Name the blood parasite species.
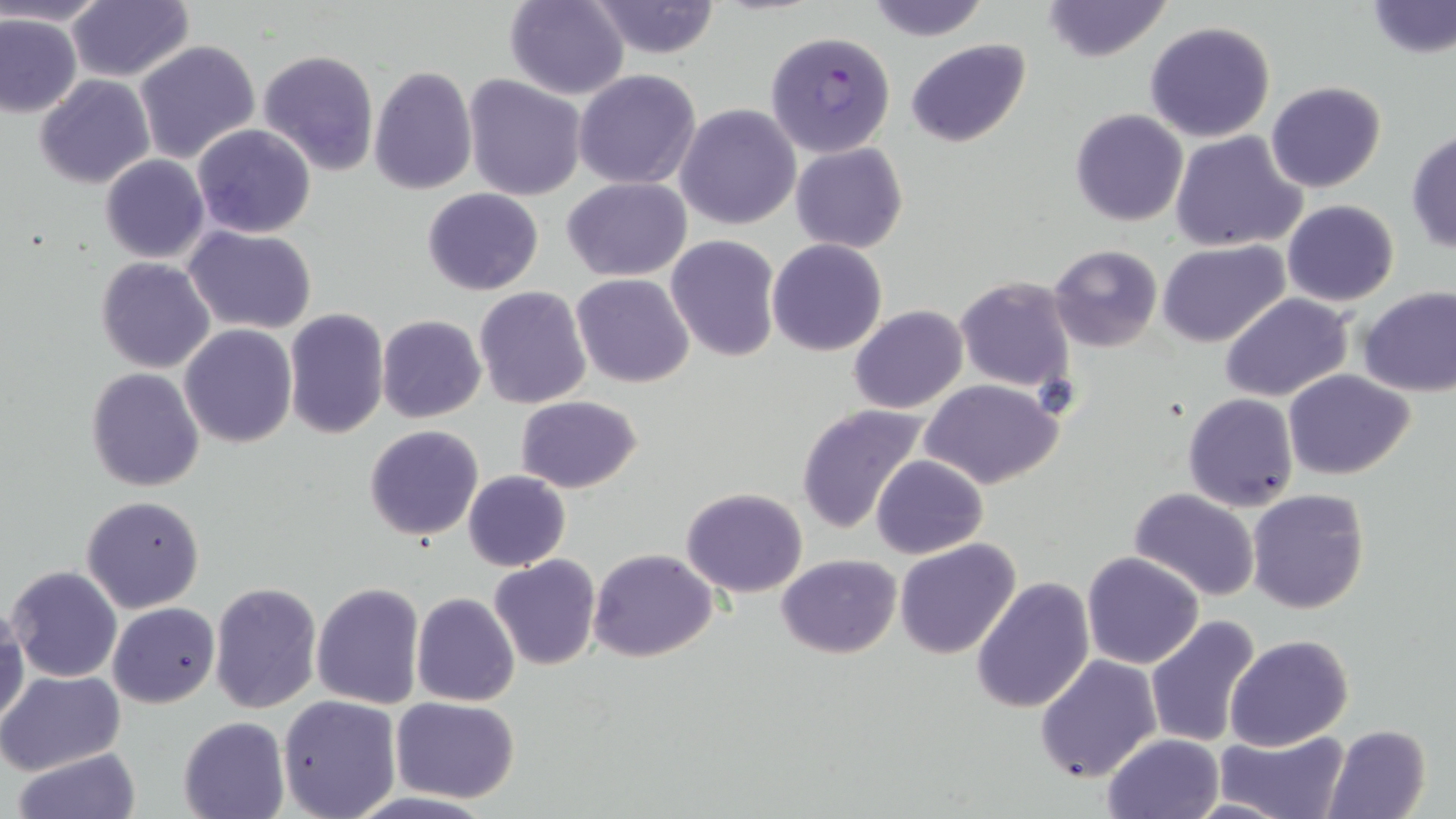

Plasmodium falciparum.

Approximate bounding boxes as named x1/y1/x2/y2 corners in pixels. Plasmodium falciparum-infected red blood cell locations: (x1=764, y1=30, x2=897, y2=160). Uninfected red blood cell locations: (x1=0, y1=0, x2=109, y2=27), (x1=503, y1=0, x2=629, y2=99), (x1=863, y1=0, x2=992, y2=42), (x1=1041, y1=0, x2=1172, y2=62), (x1=1366, y1=0, x2=1455, y2=60), (x1=586, y1=1, x2=723, y2=58), (x1=66, y1=2, x2=193, y2=83), (x1=0, y1=9, x2=82, y2=118), (x1=1144, y1=19, x2=1277, y2=142), (x1=906, y1=38, x2=1030, y2=149), (x1=133, y1=40, x2=260, y2=166), (x1=258, y1=49, x2=380, y2=175), (x1=369, y1=66, x2=477, y2=195), (x1=574, y1=69, x2=702, y2=189), (x1=35, y1=75, x2=154, y2=190), (x1=463, y1=75, x2=587, y2=201), (x1=1266, y1=80, x2=1387, y2=194), (x1=674, y1=103, x2=801, y2=230), (x1=1069, y1=108, x2=1188, y2=227), (x1=191, y1=124, x2=317, y2=239), (x1=1169, y1=129, x2=1309, y2=253), (x1=1406, y1=131, x2=1456, y2=255), (x1=790, y1=142, x2=908, y2=253), (x1=99, y1=155, x2=209, y2=264), (x1=562, y1=177, x2=692, y2=282), (x1=422, y1=188, x2=544, y2=295), (x1=1283, y1=199, x2=1398, y2=307), (x1=183, y1=225, x2=317, y2=333), (x1=666, y1=235, x2=780, y2=361), (x1=768, y1=239, x2=887, y2=356), (x1=1159, y1=240, x2=1289, y2=348), (x1=1049, y1=245, x2=1162, y2=351), (x1=96, y1=257, x2=215, y2=373), (x1=572, y1=272, x2=694, y2=388), (x1=954, y1=277, x2=1075, y2=393), (x1=1358, y1=285, x2=1456, y2=397), (x1=473, y1=286, x2=592, y2=409), (x1=1221, y1=294, x2=1351, y2=402), (x1=849, y1=305, x2=968, y2=413), (x1=283, y1=308, x2=390, y2=441), (x1=376, y1=315, x2=486, y2=423), (x1=179, y1=324, x2=299, y2=448), (x1=85, y1=368, x2=205, y2=492), (x1=1284, y1=369, x2=1415, y2=479), (x1=921, y1=378, x2=1063, y2=490), (x1=1183, y1=393, x2=1300, y2=512), (x1=515, y1=395, x2=643, y2=491), (x1=795, y1=403, x2=928, y2=534), (x1=363, y1=424, x2=485, y2=542), (x1=871, y1=453, x2=989, y2=559), (x1=464, y1=470, x2=570, y2=572), (x1=681, y1=487, x2=807, y2=598), (x1=1127, y1=488, x2=1261, y2=601), (x1=1245, y1=488, x2=1370, y2=615), (x1=80, y1=494, x2=205, y2=613), (x1=893, y1=538, x2=1021, y2=658), (x1=588, y1=548, x2=718, y2=663), (x1=1081, y1=551, x2=1206, y2=670), (x1=776, y1=553, x2=902, y2=658), (x1=488, y1=555, x2=600, y2=671), (x1=8, y1=566, x2=122, y2=683), (x1=970, y1=575, x2=1094, y2=713), (x1=311, y1=580, x2=425, y2=710), (x1=208, y1=581, x2=322, y2=716), (x1=412, y1=592, x2=520, y2=707), (x1=0, y1=600, x2=27, y2=731), (x1=107, y1=602, x2=220, y2=708), (x1=1144, y1=614, x2=1264, y2=749), (x1=1225, y1=634, x2=1352, y2=750), (x1=1034, y1=654, x2=1162, y2=781), (x1=0, y1=670, x2=125, y2=777), (x1=278, y1=695, x2=401, y2=818), (x1=392, y1=696, x2=521, y2=802), (x1=177, y1=716, x2=289, y2=819), (x1=1323, y1=723, x2=1432, y2=819), (x1=1215, y1=728, x2=1350, y2=819), (x1=1101, y1=732, x2=1225, y2=818), (x1=12, y1=746, x2=143, y2=819), (x1=1182, y1=796, x2=1293, y2=819). Image is 1456×819 pixels. Captured at 1000x magnification. Thin blood film. Single field of view. Optical microscopy. May-Grünwald-Giemsa-stained preparation.